Report the malaria status of this cell.
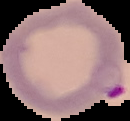
Parasitized.

From a thin blood smear. Image is 130×121 pixels. Cell region segmented out of the field of view; the surrounding area is masked to black.